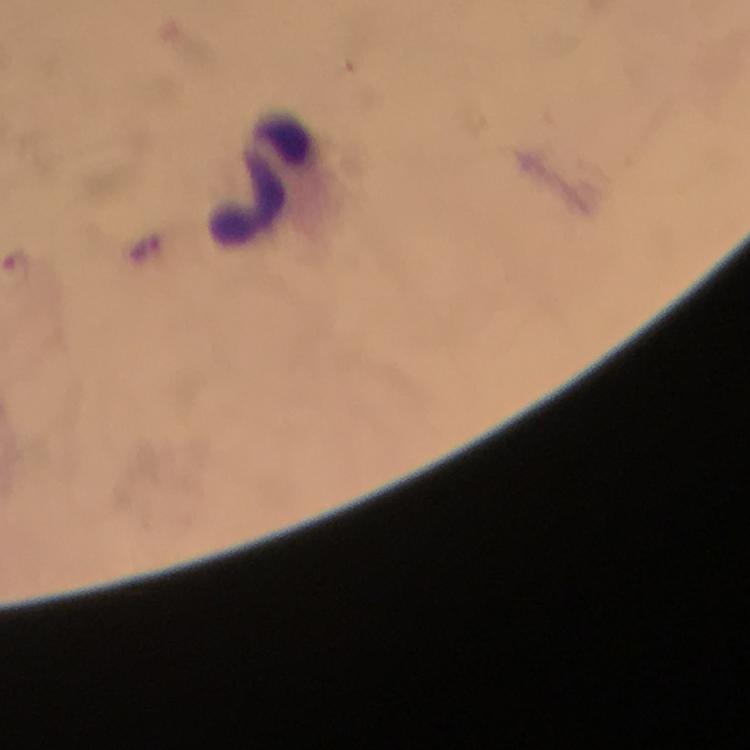

leukocyte locations = approximate object centers, in pixels from the top-left corner: (x=254, y=177)
malaria parasite locations = approximate object centers, in pixels from the top-left corner: (x=16, y=261)
preparation = thick blood smear
stain = Giemsa
context = from a diagnostic examination for malaria
cropped from = a single field of view
capture = smartphone camera through the microscope
magnification = 100x
immersion oil = applied
image size = 750×750 pixels